Assess the morphology of the red blood cells.
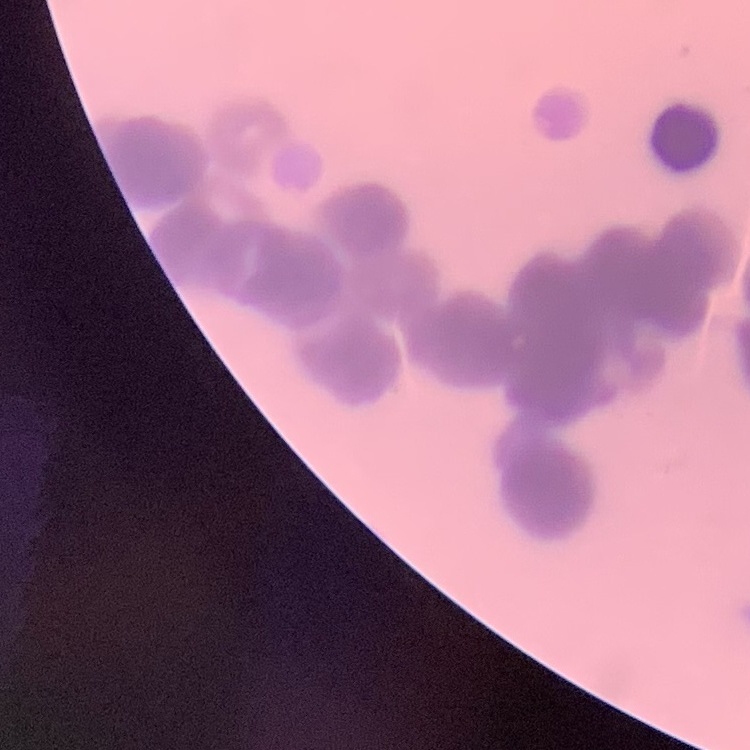
Rouleaux formation.

Thin blood film. Square crop of a larger photomicrograph. Field's or Giemsa stain.